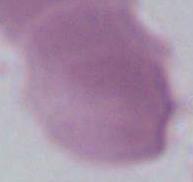

Summary:
  - Modality: micrograph
  - Identification: erythrocyte
  - Magnification: 1000x